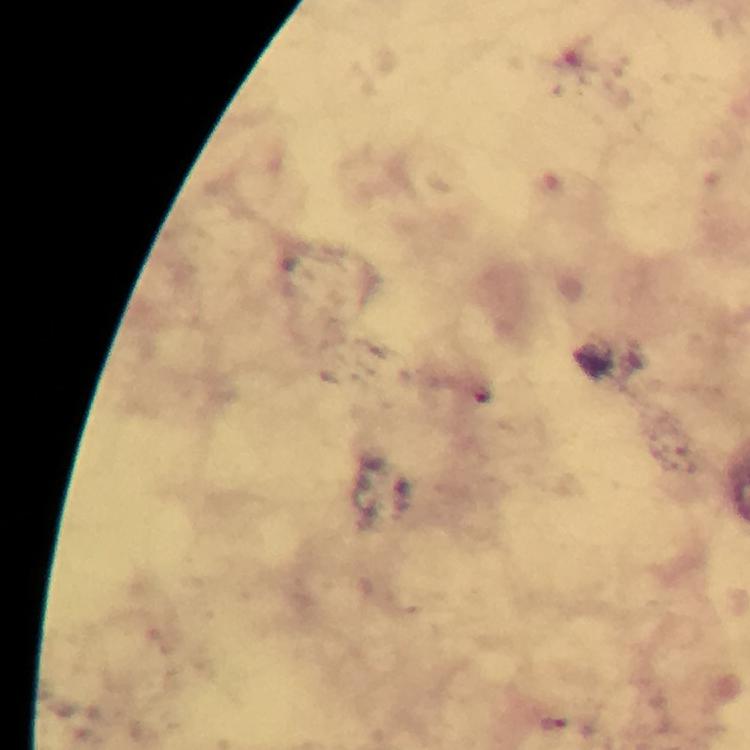
image_size: 750×750 pixels
immersion_oil: used
magnification: 100x
malaria_parasite_locations: 'approximate centers as (x, y) in pixels: (554, 727)'
stain: Giemsa
capture: smartphone mounted on the microscope
context: from a malaria diagnostic workup
cropped_from: a single field of view
preparation: thick blood film